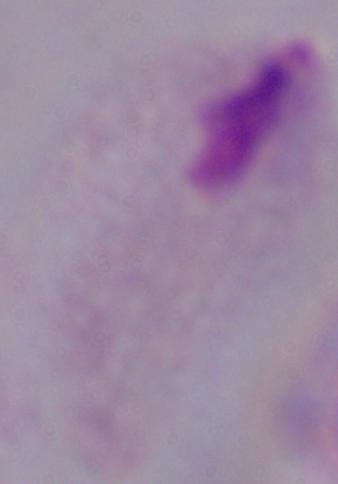

Summary:
  - Identification: trichomonad
  - Magnification: 1000x
  - Modality: micrograph